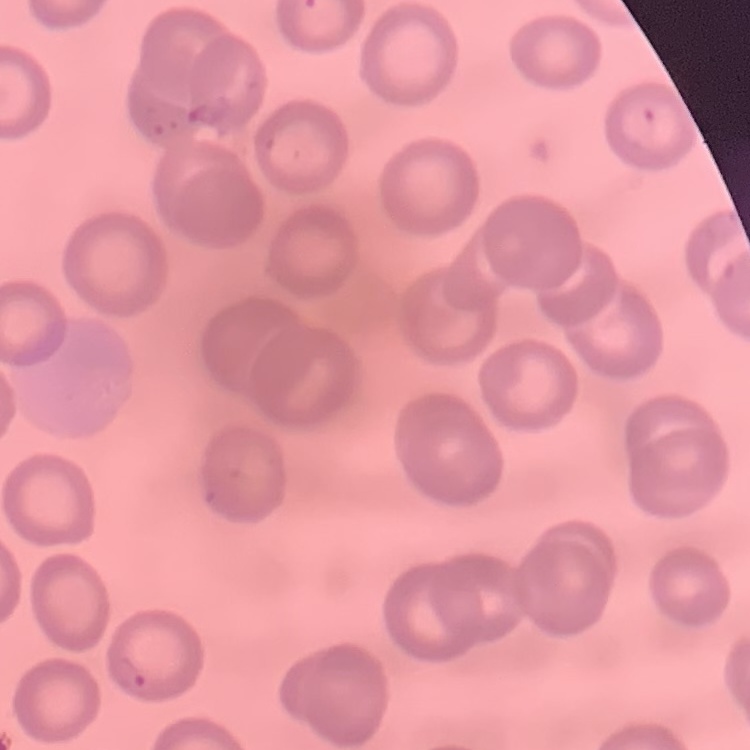

The erythrocytes exhibit no rouleaux formation. Thin blood smear. Square crop of a larger photomicrograph. Field's or Giemsa stain.